Classify this cell by malaria status.
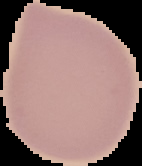
It is uninfected.

image type = segmented cell region on a black background
image size = 142×166 pixels
preparation = thin blood film